Name the cell type shown.
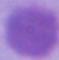

This is an erythrocyte.

Captured at 1000x magnification. Photomicrograph.